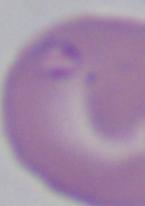

Summary:
  - Identification: Babesia
  - Magnification: 1000x
  - Modality: photomicrograph